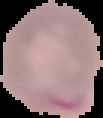
image size = 103×118 pixels
preparation = thin blood film
image type = segmented cell region with the area outside set to black
malaria status = parasitized